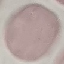

Summary:
  - Result: no malaria parasites seen
  - Stain: Giemsa
  - Image type: automatically extracted cell patch, resized to 64 × 64 pixels
  - Capture: smartphone through the microscope eyepiece
  - Preparation: thin blood smear